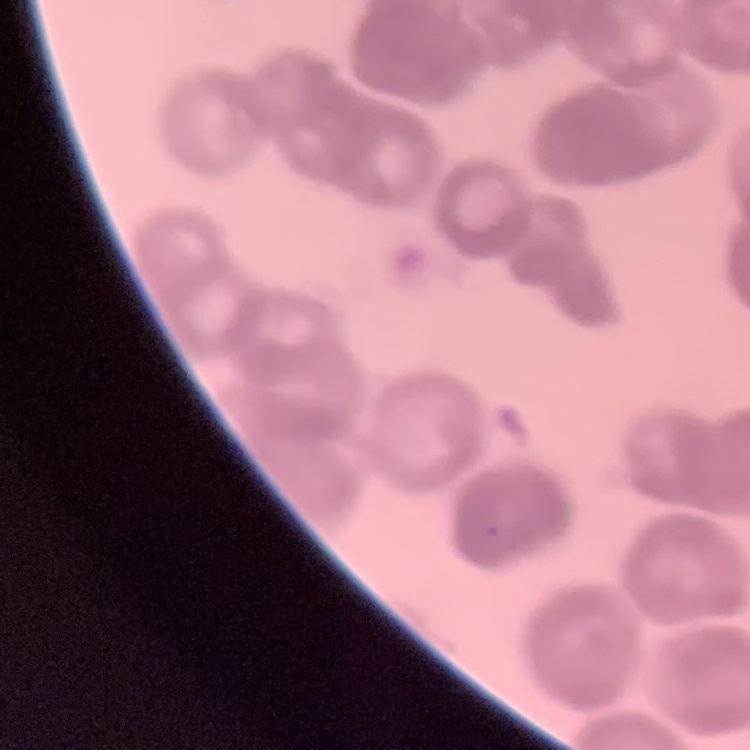 The red blood cells show rouleaux formation. Square crop of a larger photomicrograph. Thin blood smear. Stained with either Field's or Giemsa.